Assess this cell for malaria.
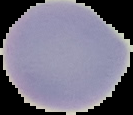
Uninfected.

Image is 133×115 pixels. From a thin blood film. Segmented cell region on a black background.